Evaluate for Plasmodium parasites.
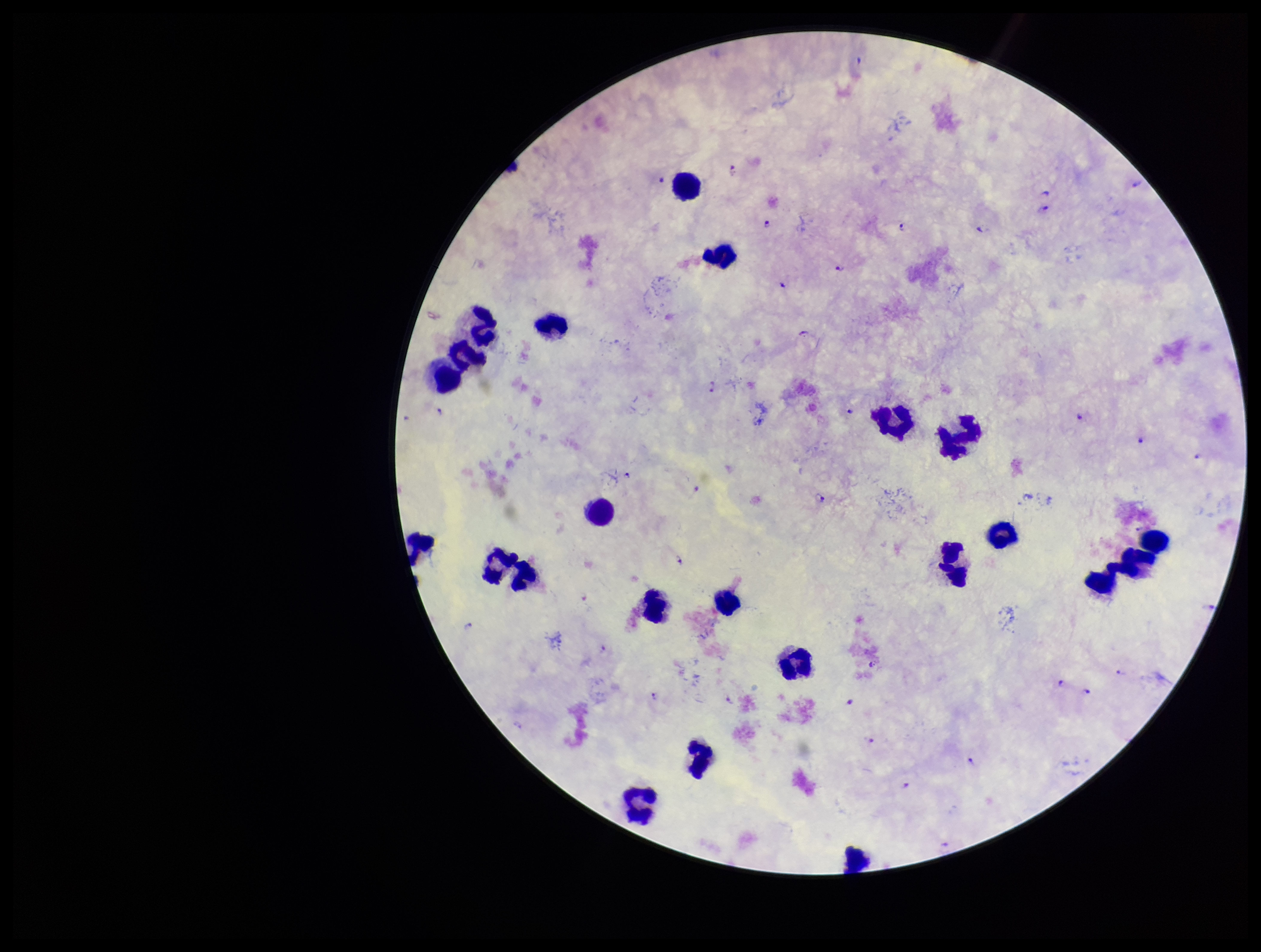
Seen.

Parasite count: 32. Stained with Giemsa. Patient malaria status: positive. Preparation: thick. One field from this slide. Species reported for this patient: Plasmodium falciparum. Smartphone photograph taken through the eyepiece of a microscope. Leukocyte count: 22. Image is 1261×952 pixels.